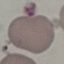
Summary:
  - Malaria status: uninfected
  - Image type: automatically extracted cell patch, resized to 64 × 64 pixels
  - Capture: smartphone through the microscope eyepiece
  - Stain: Giemsa
  - Preparation: thin blood smear